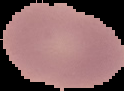 From a thin blood film. Result: negative for Plasmodium parasites. Image is 124×91 pixels. Segmented cell region on a black background.